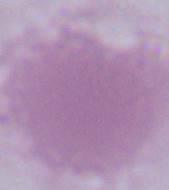 Photomicrograph. 1000x magnification. A red blood cell is seen.